Report the malaria status of this cell.
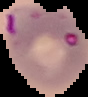
It is parasitized.

Image is 88×97 pixels. From a thin blood smear. Segmented cell region on a black background.